Identify the blood parasite species.
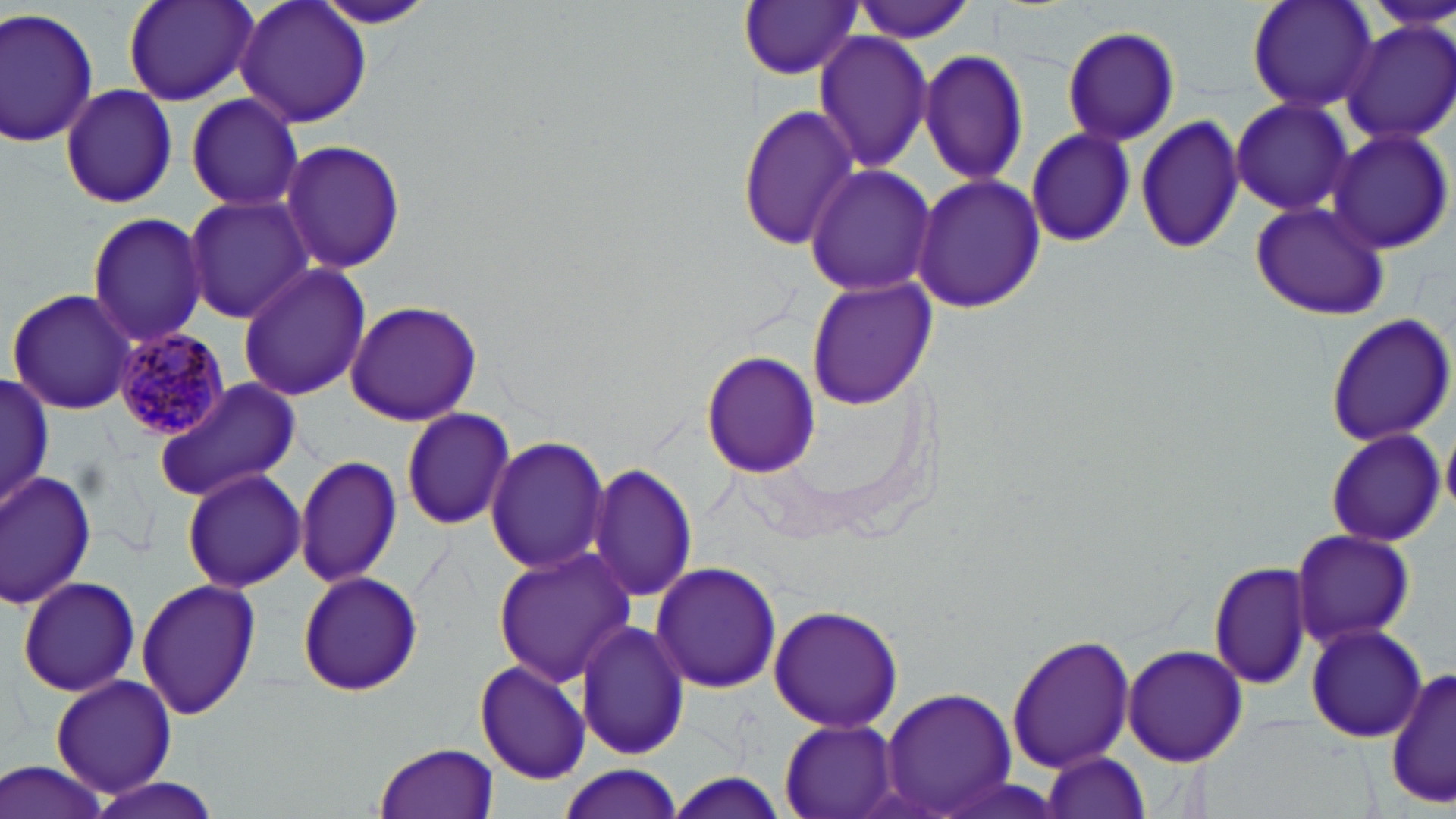

Plasmodium malariae.

Summary:
  - Coordinate format: approximate bounding boxes as [x1, y1, x2, y2] in pixels
  - Plasmodium malariae-infected red blood cell locations: [111, 326, 231, 440]
  - Uninfected red blood cell locations: [122, 0, 259, 108], [234, 0, 374, 130], [308, 0, 439, 29], [739, 0, 861, 80], [854, 0, 979, 43], [1245, 0, 1378, 116], [0, 6, 100, 149], [1341, 18, 1456, 144], [1063, 26, 1181, 145], [812, 29, 935, 176], [918, 50, 1030, 188], [60, 83, 178, 209], [182, 94, 303, 211], [1230, 97, 1355, 216], [738, 102, 859, 252], [1134, 115, 1247, 255], [1025, 127, 1136, 247], [1329, 129, 1454, 255], [279, 139, 408, 272], [803, 163, 937, 298], [912, 172, 1045, 315], [181, 193, 312, 323], [1248, 201, 1390, 321], [84, 211, 211, 348], [236, 263, 373, 400], [808, 278, 935, 410], [6, 286, 138, 416], [342, 299, 483, 427], [1324, 312, 1456, 446], [700, 351, 820, 478], [1, 373, 55, 513], [154, 376, 301, 503], [400, 406, 516, 532], [1442, 422, 1456, 519], [1325, 427, 1447, 548], [486, 436, 609, 578], [294, 454, 402, 588], [587, 463, 700, 607], [181, 467, 306, 593], [0, 470, 100, 610], [1289, 529, 1416, 649], [492, 548, 633, 688], [1208, 560, 1314, 690], [650, 561, 781, 694], [297, 570, 424, 697], [16, 575, 142, 699], [136, 577, 261, 723], [766, 602, 906, 734], [576, 620, 688, 760], [1306, 623, 1427, 742], [1006, 632, 1136, 774], [1122, 643, 1247, 766], [475, 659, 591, 784], [1388, 666, 1455, 809], [50, 674, 177, 798], [879, 686, 1020, 817], [778, 719, 901, 819], [373, 743, 500, 819], [1037, 749, 1153, 819], [0, 761, 111, 819], [557, 765, 683, 819], [661, 771, 791, 818], [86, 776, 221, 819]
  - Modality: optical microscopy
  - Stain: May-Grünwald-Giemsa
  - Field of view: one of a larger specimen
  - Image size: 1456×819 pixels
  - Preparation: thin blood film
  - Magnification: 1000x